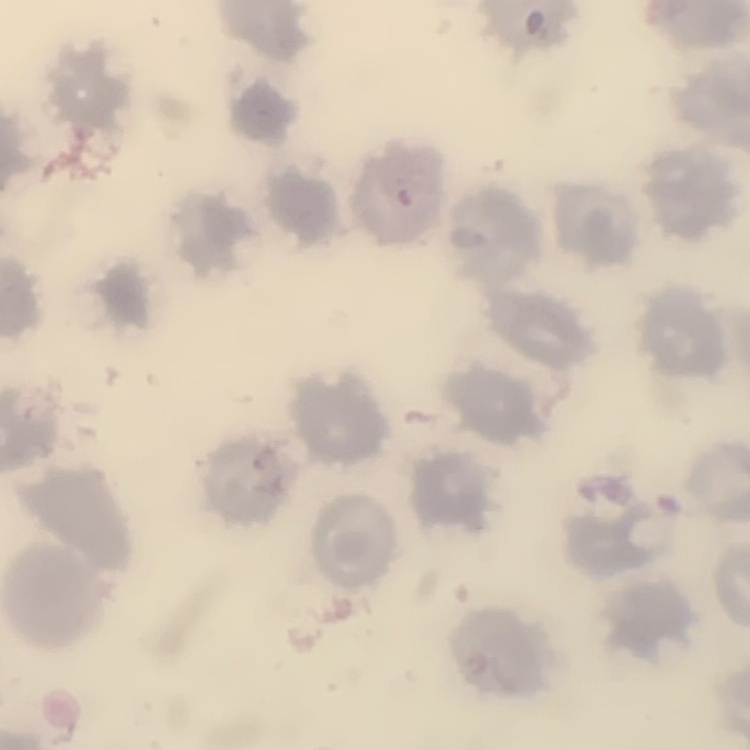

red blood cell morphology = no rouleaux formation
image type = one tile cut from a larger photomicrograph
preparation = thin blood film
stain = Field's or Giemsa